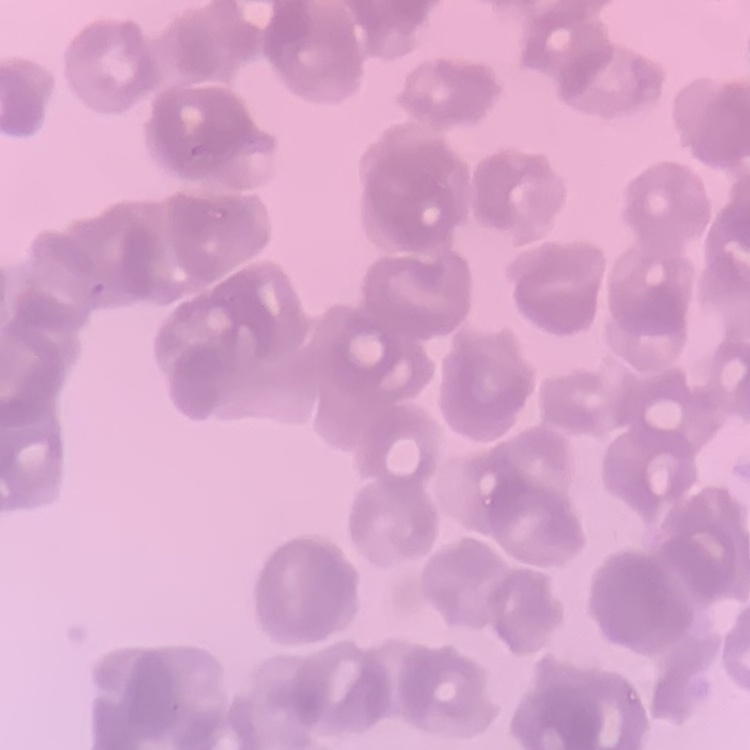
Summary:
  - Erythrocyte morphology: rouleaux formation
  - Image type: one tile cut from a larger photomicrograph
  - Preparation: thin blood smear
  - Stain: Field's or Giemsa